Identify the blood parasite species.
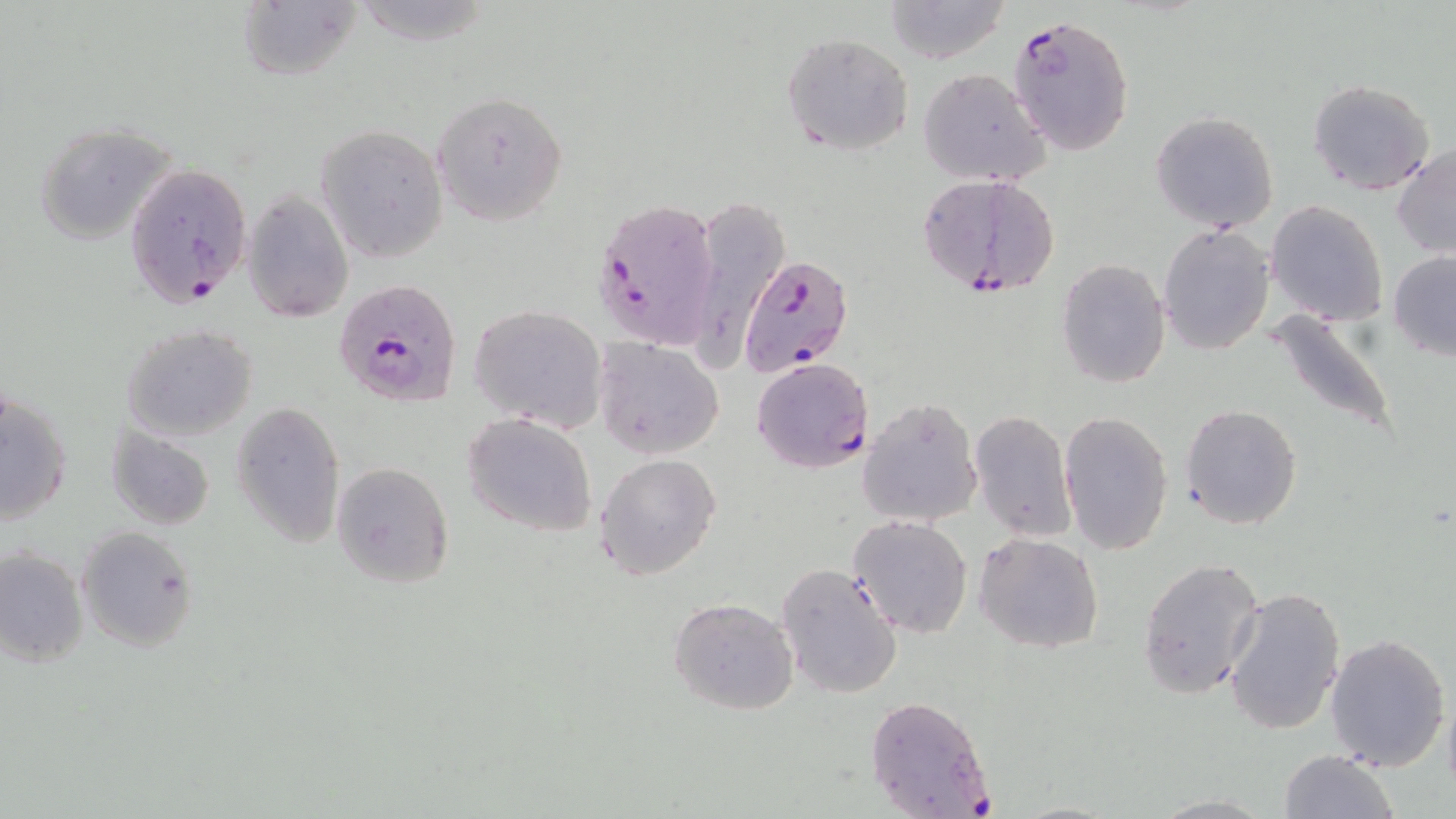
Plasmodium falciparum.

Approximate bounding boxes as (x1,y1)-(x2,y2) corner pairs in pixels. Plasmodium falciparum-infected red blood cell locations: (1008,13)-(1134,155), (124,160)-(253,306), (920,172)-(1062,297), (594,194)-(720,349), (738,253)-(851,380), (336,281)-(460,406), (751,358)-(872,473), (863,695)-(998,816). Uninfected red blood cell locations: (882,0)-(1013,64), (237,1)-(360,82), (782,32)-(913,156), (920,68)-(1049,187), (1306,79)-(1436,196), (432,90)-(568,226), (1151,111)-(1278,231), (33,121)-(182,245), (317,125)-(447,262), (1392,144)-(1456,259), (242,187)-(355,323), (1266,201)-(1386,324), (692,202)-(794,369), (1157,224)-(1274,356), (1387,251)-(1456,362), (1056,259)-(1172,389), (469,305)-(607,432), (1264,309)-(1401,441), (122,323)-(259,442), (594,338)-(724,460), (1,390)-(73,527), (857,395)-(983,526), (230,399)-(345,548), (1180,405)-(1302,530), (970,409)-(1077,542), (1060,410)-(1174,555), (464,414)-(598,537), (107,427)-(215,530), (595,454)-(721,581), (330,462)-(455,589), (849,515)-(973,637), (77,526)-(199,651), (975,532)-(1104,654), (1,546)-(88,668), (1138,556)-(1265,698), (776,564)-(903,699), (1223,585)-(1345,737), (670,598)-(798,715), (1324,632)-(1452,772), (1278,748)-(1400,819), (1144,792)-(1278,817). Thin blood film. Image is 1456×819 pixels. Captured at 1000x magnification. One field of a larger specimen. May-Grünwald-Giemsa stain. Light microscopy.